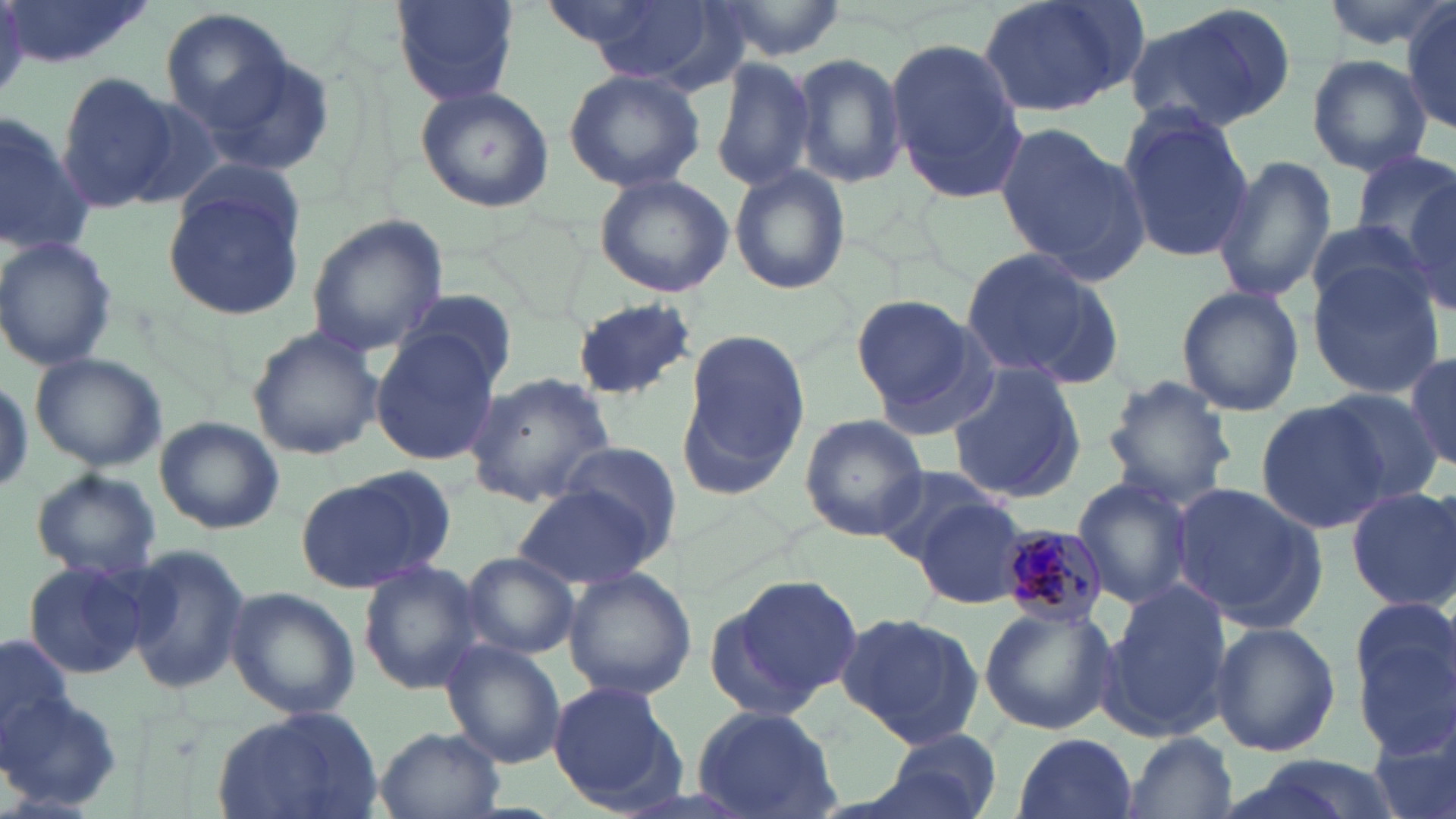
Summary:
  - Coordinate format: approximate bounding boxes as (x1,y1)-(x2,y2) corner pairs in pixels
  - Plasmodium malariae-infected red blood cell locations: (1000,524)-(1109,630)
  - Uninfected red blood cell locations: (5,0)-(156,70), (391,0)-(518,106), (558,0)-(727,79), (702,0)-(847,65), (974,0)-(1148,119), (1318,0)-(1453,50), (1124,3)-(1296,134), (1401,5)-(1456,136), (160,7)-(297,138), (885,39)-(1027,202), (792,52)-(907,186), (1308,55)-(1431,175), (201,56)-(338,180), (711,56)-(816,193), (562,68)-(706,193), (54,73)-(185,213), (414,86)-(556,212), (1116,108)-(1253,261), (0,112)-(92,257), (993,122)-(1144,279), (1350,149)-(1456,263), (1209,155)-(1336,306), (729,166)-(850,296), (594,172)-(736,298), (1404,178)-(1456,313), (163,181)-(306,322), (305,214)-(447,359), (1303,223)-(1433,320), (0,237)-(118,369), (958,244)-(1122,387), (1307,264)-(1444,396), (1175,284)-(1305,416), (397,288)-(516,391), (852,294)-(987,420), (569,297)-(696,400), (247,325)-(382,461), (677,332)-(806,497), (369,334)-(500,465), (29,351)-(168,472), (1406,355)-(1455,470), (945,362)-(1088,503), (462,374)-(617,507), (1101,375)-(1238,508), (1321,386)-(1444,507), (1259,397)-(1394,533), (798,414)-(929,540), (155,416)-(284,534), (558,441)-(684,553), (872,465)-(1005,568), (299,468)-(453,592), (30,469)-(161,580), (1071,477)-(1195,610), (512,481)-(664,591), (1171,481)-(1328,631), (1345,484)-(1456,610), (914,498)-(1028,611), (120,545)-(254,696), (460,551)-(580,660), (22,558)-(155,681), (357,560)-(486,694), (563,569)-(696,698), (708,574)-(863,719), (1096,579)-(1235,739), (225,588)-(360,720), (1350,595)-(1456,754), (978,603)-(1116,736), (836,611)-(984,748), (1210,621)-(1341,759), (0,633)-(74,755), (439,640)-(566,766), (547,681)-(681,810), (1,690)-(125,811), (691,705)-(843,819), (212,708)-(383,819), (1369,710)-(1456,819), (878,726)-(1004,819), (374,727)-(506,818), (1013,732)-(1138,818), (1123,732)-(1239,818)
  - Slide-level diagnosis: Plasmodium malariae
  - Image size: 1456×819 pixels
  - Preparation: thin blood smear
  - Modality: optical microscopy
  - Field of view: one of a larger specimen
  - Magnification: 1000x
  - Stain: May-Grünwald-Giemsa